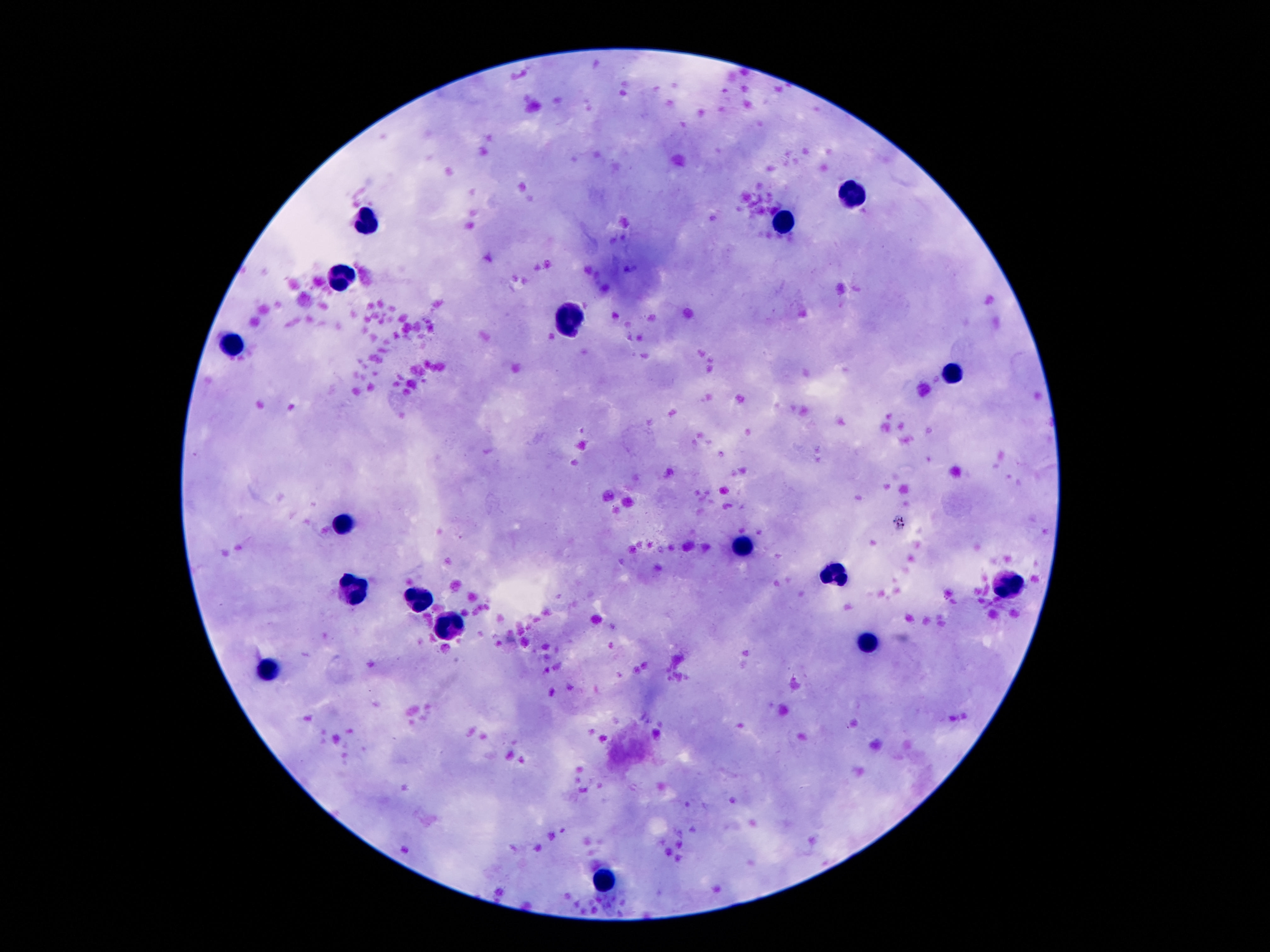 Approximate centers as (x, y) in pixels. Leukocyte locations: (850, 196), (364, 225), (784, 225), (346, 275), (573, 318), (237, 339), (955, 372), (346, 518), (741, 548), (834, 577), (1005, 586), (353, 589), (416, 598), (441, 626), (866, 643), (269, 667), (605, 884). Giemsa stain. Photographed through the microscope eyepiece with a smartphone camera. Thick blood smear. 100x magnification. Patient malaria status: negative. Image is 1270×952 pixels. One field from this slide.